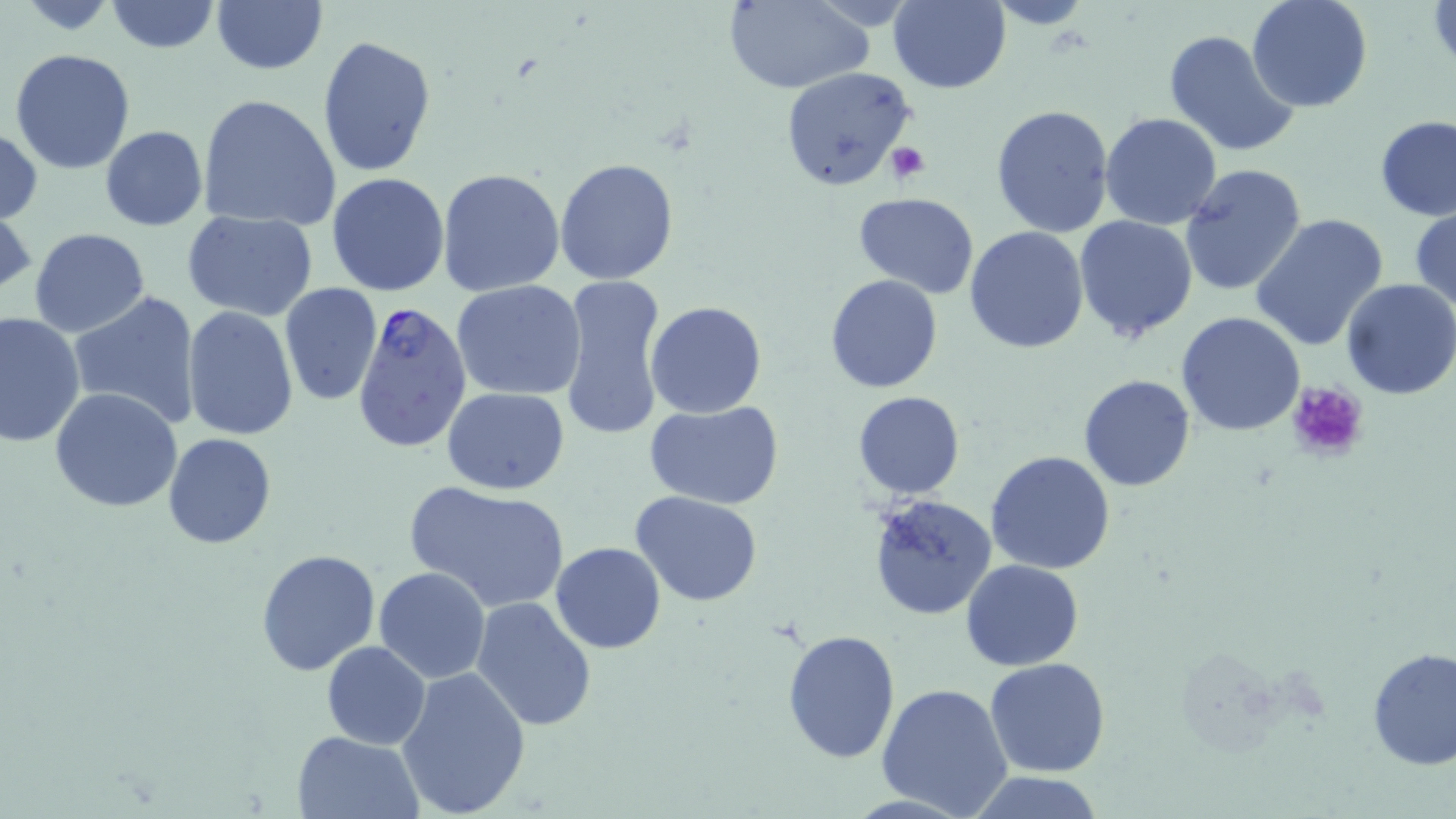

slide_level_diagnosis: Plasmodium falciparum
uninfected_red_blood_cell_locations: 'approximate bounding boxes as named x1/y1/x2/y2 corners in pixels: (x1=102, y1=0, x2=221, y2=53), (x1=887, y1=0, x2=1011, y2=93), (x1=1245, y1=0, x2=1373, y2=113), (x1=211, y1=1, x2=328, y2=76), (x1=721, y1=1, x2=872, y2=93), (x1=986, y1=1, x2=1097, y2=29), (x1=1427, y1=1, x2=1455, y2=72), (x1=1162, y1=29, x2=1301, y2=158), (x1=318, y1=33, x2=438, y2=177), (x1=9, y1=48, x2=137, y2=176), (x1=778, y1=65, x2=916, y2=193), (x1=198, y1=93, x2=341, y2=231), (x1=989, y1=103, x2=1115, y2=240), (x1=1100, y1=112, x2=1222, y2=229), (x1=1376, y1=116, x2=1456, y2=220), (x1=0, y1=125, x2=43, y2=226), (x1=100, y1=126, x2=208, y2=231), (x1=553, y1=157, x2=679, y2=286), (x1=1179, y1=164, x2=1308, y2=299), (x1=437, y1=168, x2=566, y2=297), (x1=325, y1=172, x2=451, y2=297), (x1=853, y1=191, x2=981, y2=298), (x1=1410, y1=205, x2=1456, y2=314), (x1=181, y1=210, x2=318, y2=320), (x1=1250, y1=212, x2=1390, y2=352), (x1=1074, y1=215, x2=1199, y2=342), (x1=963, y1=226, x2=1090, y2=353), (x1=30, y1=227, x2=150, y2=337), (x1=825, y1=273, x2=943, y2=393), (x1=557, y1=275, x2=669, y2=442), (x1=1341, y1=278, x2=1456, y2=400), (x1=452, y1=280, x2=587, y2=403), (x1=280, y1=284, x2=383, y2=405), (x1=69, y1=291, x2=200, y2=430), (x1=646, y1=302, x2=766, y2=418), (x1=182, y1=305, x2=300, y2=440), (x1=0, y1=309, x2=86, y2=447), (x1=1177, y1=310, x2=1305, y2=436), (x1=1078, y1=374, x2=1196, y2=492), (x1=49, y1=386, x2=184, y2=515), (x1=441, y1=387, x2=568, y2=495), (x1=853, y1=390, x2=966, y2=500), (x1=645, y1=401, x2=785, y2=509), (x1=165, y1=434, x2=276, y2=548), (x1=984, y1=450, x2=1116, y2=575), (x1=404, y1=481, x2=571, y2=614), (x1=631, y1=492, x2=766, y2=607), (x1=868, y1=495, x2=996, y2=618), (x1=551, y1=541, x2=666, y2=653), (x1=256, y1=549, x2=382, y2=676), (x1=960, y1=559, x2=1085, y2=672), (x1=374, y1=566, x2=491, y2=683), (x1=471, y1=596, x2=598, y2=734), (x1=782, y1=627, x2=901, y2=764), (x1=323, y1=641, x2=430, y2=749), (x1=1366, y1=646, x2=1456, y2=770), (x1=985, y1=657, x2=1111, y2=776), (x1=397, y1=666, x2=532, y2=817), (x1=876, y1=682, x2=1014, y2=818), (x1=293, y1=731, x2=423, y2=819), (x1=965, y1=772, x2=1108, y2=817)'
magnification: 1000x
stain: May-Grünwald-Giemsa
field_of_view: single
preparation: thin blood smear
plasmodium_falciparum_infected_red_blood_cell_locations: 'approximate bounding boxes as named x1/y1/x2/y2 corners in pixels: (x1=352, y1=302, x2=472, y2=454)'
platelet_locations: 'approximate bounding boxes as named x1/y1/x2/y2 corners in pixels: (x1=886, y1=143, x2=929, y2=183), (x1=1286, y1=380, x2=1367, y2=460)'
modality: optical microscopy
image_size: 1456×819 pixels